State which parasite is depicted.
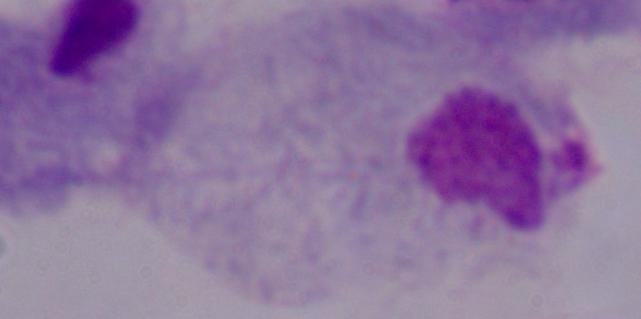

This is a trichomonad.

Photomicrograph. Captured at 1000x magnification.